Classify the preparation.
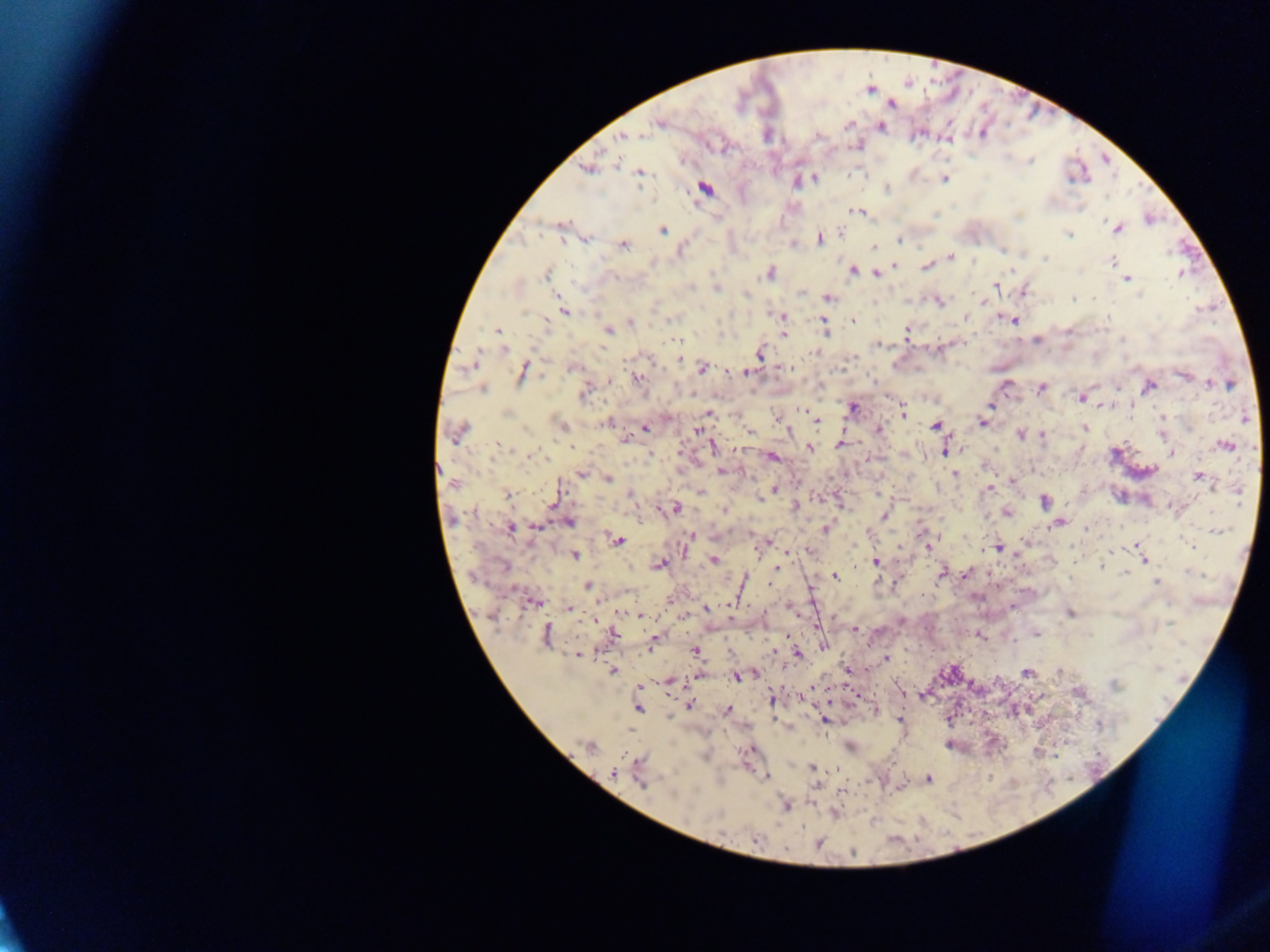
Thick blood smear.

Approximate centers as (x, y) in pixels. Malaria parasite locations: (869, 89), (890, 103), (659, 122), (848, 125), (879, 126), (920, 132), (622, 137), (945, 138), (857, 144), (587, 168), (638, 172), (945, 178), (813, 179), (797, 180), (704, 189), (859, 211), (561, 225), (1117, 228), (663, 229), (1066, 233), (585, 238), (819, 238), (898, 239), (792, 243), (622, 244), (873, 248), (1002, 249), (950, 256), (1045, 258), (1113, 262), (894, 264), (927, 265), (853, 269), (769, 272), (875, 272), (1180, 273), (547, 274), (1126, 278), (995, 284), (716, 288), (1022, 291), (1074, 297), (827, 298), (938, 301), (563, 311), (781, 316), (964, 316), (852, 320), (1014, 320), (631, 322), (544, 323), (823, 325), (607, 330), (498, 332), (826, 333), (906, 333), (782, 334), (678, 339), (1037, 339), (877, 343), (504, 348), (939, 348), (816, 352), (759, 353), (678, 359), (473, 363), (573, 367), (702, 368), (784, 369), (524, 370), (746, 371), (1184, 374), (636, 378), (609, 380), (1212, 383), (1228, 384), (820, 385), (1005, 385), (1148, 386), (1041, 387), (482, 388), (586, 389), (1081, 397), (990, 405), (1102, 406), (851, 408), (805, 409), (708, 412), (902, 412), (1162, 417), (777, 418), (1245, 418), (816, 420), (607, 422), (981, 422), (936, 425), (561, 426), (644, 427), (878, 428), (1084, 428), (697, 430), (458, 431), (749, 431), (1163, 433), (1021, 434), (1042, 434), (623, 439), (840, 444), (1226, 445), (570, 446), (712, 446), (810, 448), (945, 449), (650, 454), (1170, 454), (529, 456), (772, 457), (720, 470), (581, 473), (956, 474), (1197, 475), (607, 478), (1013, 480), (454, 483), (988, 488), (773, 489), (1237, 489), (701, 492), (878, 493), (508, 494), (631, 494), (759, 498), (1044, 502), (553, 503), (840, 503), (795, 507), (674, 508), (724, 510), (1005, 512), (883, 516), (569, 521), (1058, 523), (537, 526), (509, 528), (826, 529), (1215, 530), (749, 533), (690, 538), (617, 541), (767, 542), (1137, 545), (686, 546), (928, 546), (997, 548), (808, 550), (1141, 550), (788, 552), (574, 554), (713, 559), (1050, 559), (1144, 559), (876, 561), (659, 565), (504, 566), (776, 568), (941, 572), (966, 572), (1123, 572), (835, 577), (742, 580), (1155, 581), (769, 582), (588, 585), (533, 601), (789, 606), (1012, 606), (569, 608), (706, 608), (1069, 613), (638, 614), (853, 629), (612, 633), (1036, 633), (978, 634), (547, 635), (788, 636), (652, 641), (822, 646), (694, 650), (773, 651), (578, 654), (797, 655), (886, 660), (846, 668), (613, 670), (1027, 672), (1059, 672), (752, 673), (697, 675), (736, 675), (668, 681), (1114, 685), (638, 687), (900, 690), (1078, 692), (855, 694), (800, 695), (922, 696), (771, 699), (689, 705), (637, 708), (726, 710), (874, 710), (901, 718), (824, 720), (1099, 724), (849, 745), (948, 745), (588, 747), (748, 749), (1035, 752), (811, 767), (614, 772), (639, 772), (766, 776), (928, 778), (815, 783), (841, 790), (785, 806), (835, 813), (755, 840), (818, 842). Single field of view. Collected in Ghana. Image is 1270×952 pixels. Photographed through a microscope with a mobile-phone camera.